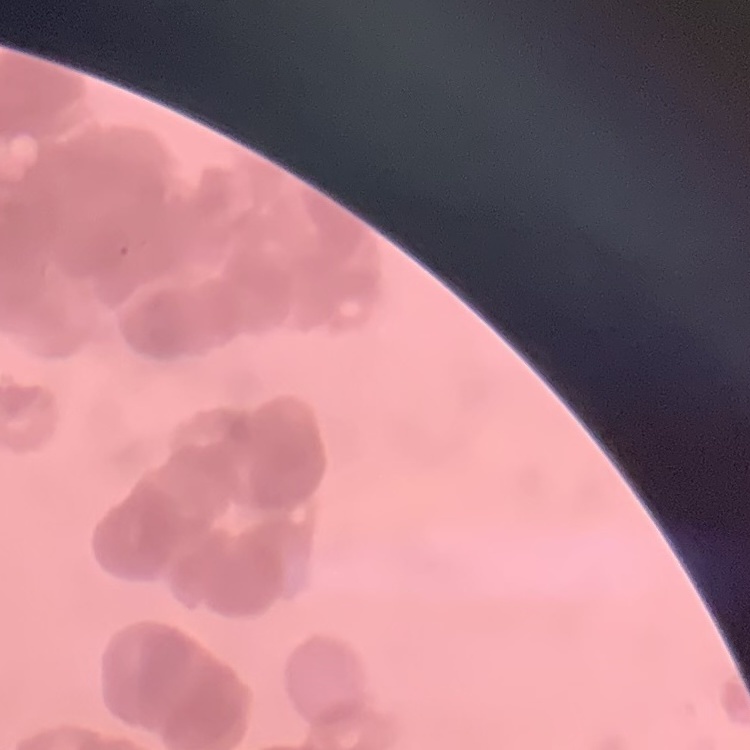
Summary:
  - Red blood cell morphology: rouleaux formation
  - Image type: one tile cut from a larger photomicrograph
  - Stain: Field's or Giemsa
  - Preparation: thin blood smear